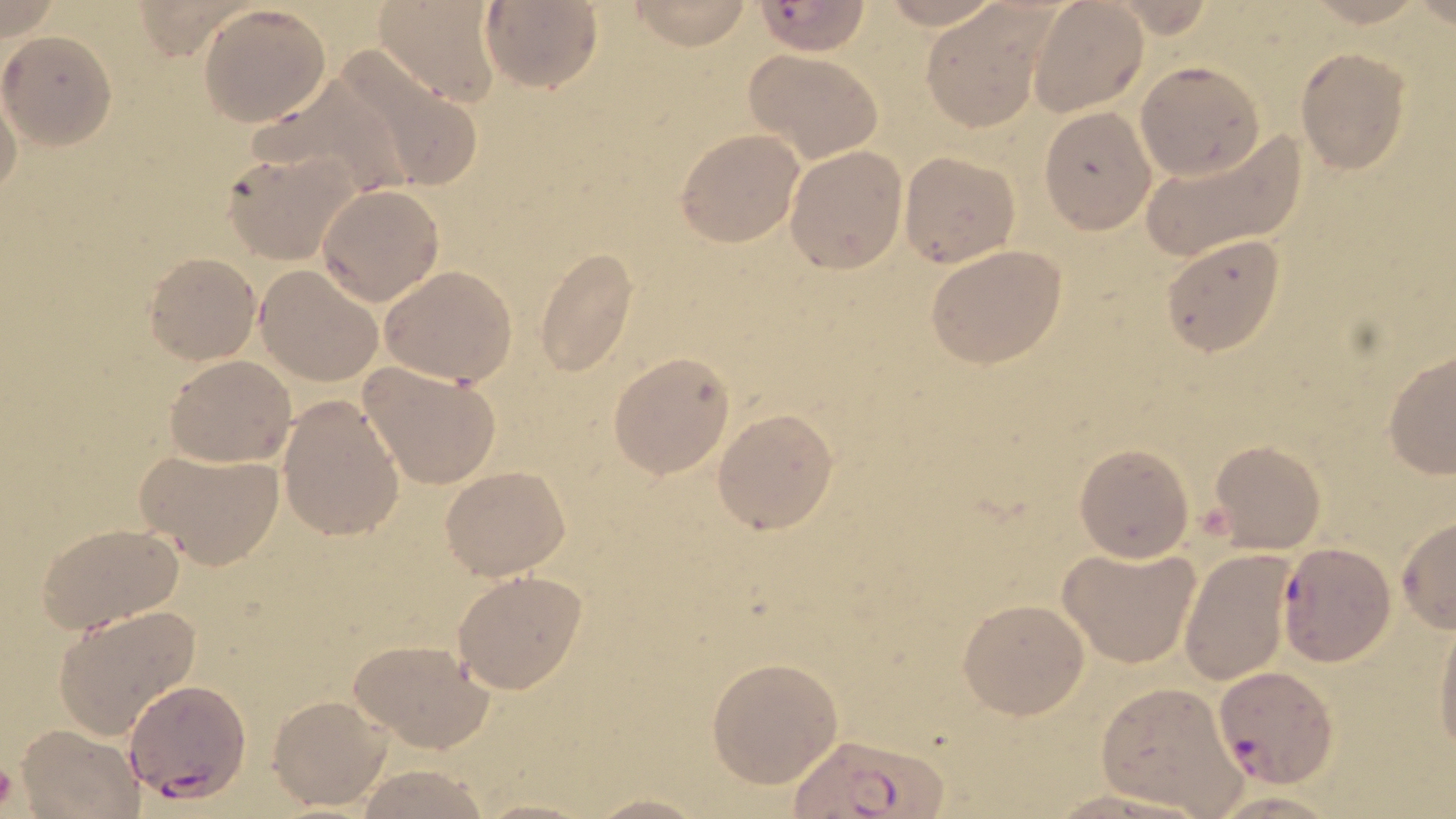

slide-level diagnosis = Plasmodium falciparum
modality = optical microscopy
field of view = one of a larger specimen
platelet locations = approximate bounding boxes as (x1,y1)-(x2,y2) corner pairs in pixels: (0,757)-(17,813)
uninfected red blood cell locations = approximate bounding boxes as (x1,y1)-(x2,y2) corner pairs in pixels: (372,0)-(503,106), (479,0)-(603,93), (876,0)-(1007,33), (626,1)-(754,49), (1028,1)-(1149,115), (198,4)-(331,127), (922,8)-(1052,131), (0,31)-(116,147), (1295,47)-(1412,173), (331,48)-(485,193), (744,50)-(884,163), (1135,60)-(1267,182), (1,86)-(24,203), (1037,107)-(1157,233), (675,129)-(805,246), (1140,129)-(1306,264), (784,144)-(908,274), (221,148)-(358,263), (899,151)-(1019,268), (318,184)-(444,306), (1159,234)-(1286,356), (926,244)-(1069,369), (533,245)-(640,378), (145,251)-(261,364), (255,266)-(382,386), (379,266)-(517,386), (608,352)-(734,478), (165,356)-(296,466), (1381,356)-(1456,476), (357,361)-(502,490), (277,394)-(402,542), (713,409)-(838,535), (1208,439)-(1326,553), (1074,443)-(1194,562), (135,446)-(285,570), (440,465)-(572,580), (1395,518)-(1456,632), (36,520)-(185,634), (1057,543)-(1201,669), (1179,547)-(1294,687), (452,570)-(588,694), (958,599)-(1091,719), (53,605)-(201,738), (1433,613)-(1456,760), (347,638)-(495,752), (706,657)-(843,787), (1096,681)-(1249,817), (268,693)-(390,812), (16,724)-(144,817), (353,766)-(492,818), (1052,788)-(1215,819), (1204,789)-(1345,818), (578,794)-(720,817)
Plasmodium falciparum-infected red blood cell locations = approximate bounding boxes as (x1,y1)-(x2,y2) corner pairs in pixels: (754,2)-(877,53), (1277,541)-(1394,665), (1212,665)-(1337,788), (125,679)-(250,802), (791,735)-(949,819)
preparation = thin blood smear
stain = May-Grünwald-Giemsa
image size = 1456×819 pixels
magnification = 1000x